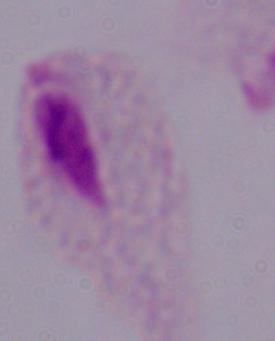
Photomicrograph. A trichomonad is shown. Captured at 1000x magnification.